Identify the parasite.
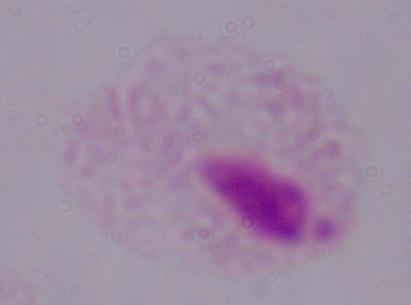
A trichomonad.

magnification = 1000x
modality = photomicrograph